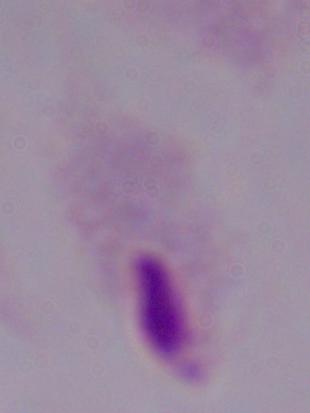

Captured at 1000x magnification. Micrograph. A trichomonad is seen.